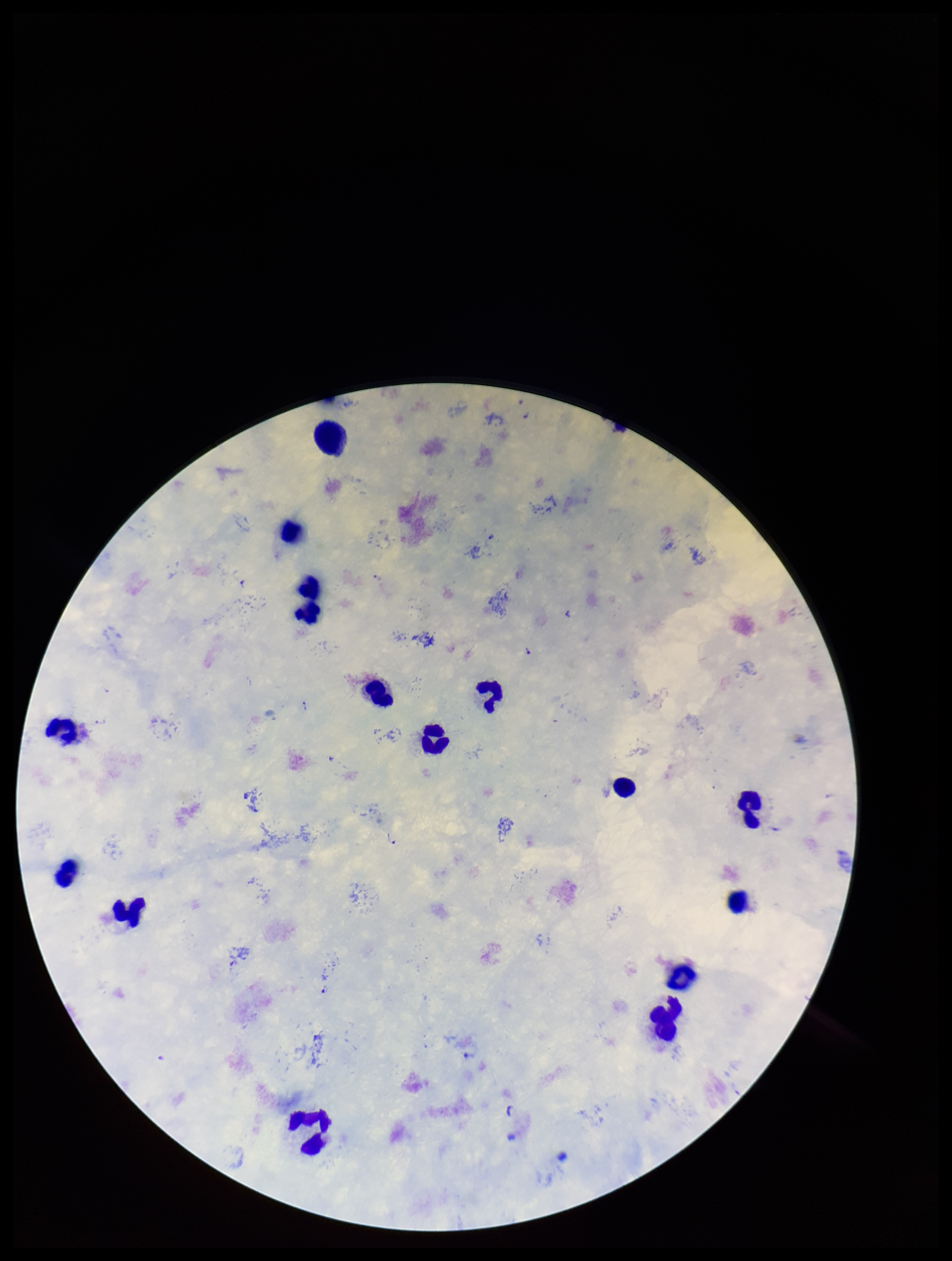
One field from this slide. Leukocyte count: 15. Species reported for this patient: Plasmodium falciparum. Parasite count: 6. Image is 952×1261 pixels. Stained with Giemsa. Preparation: thick blood smear. Plasmodium parasites: detected. Patient malaria status: positive. Smartphone photograph taken through the eyepiece of a microscope.